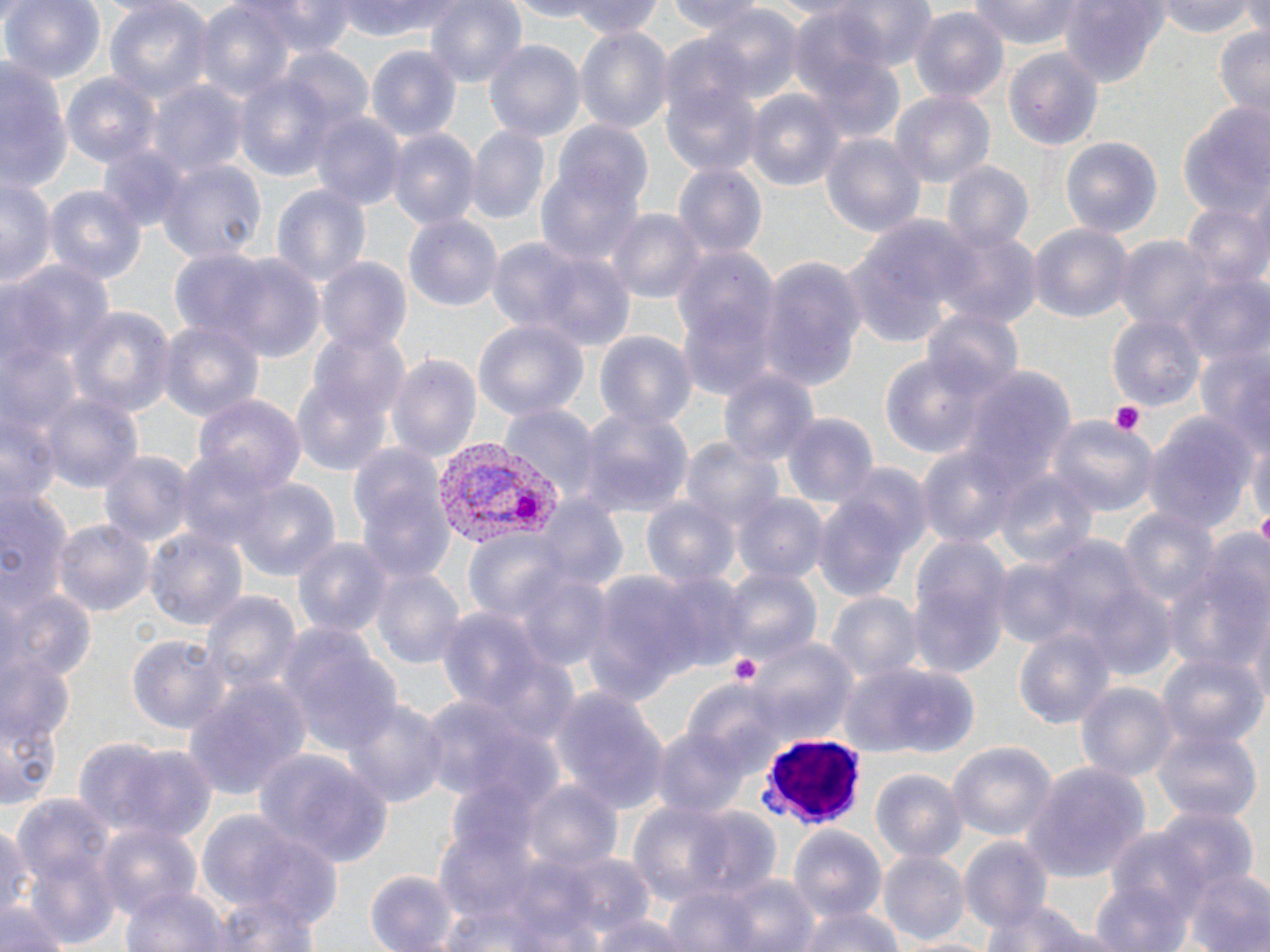
Summary:
  - Coordinate format: approximate bounding boxes as (x1, y1, x2, y2) in pixels
  - White blood cell locations: (763, 737, 868, 828)
  - Platelet locations: (1108, 399, 1145, 436), (1255, 510, 1270, 545), (727, 652, 765, 690)
  - Plasmodium vivax-infected red blood cell locations: (428, 436, 568, 551)
  - Uninfected red blood cell locations: (2, 0, 106, 85), (102, 0, 212, 106), (193, 0, 296, 104), (241, 0, 359, 56), (336, 0, 472, 42), (424, 0, 530, 90), (500, 0, 605, 20), (567, 0, 667, 39), (667, 0, 769, 37), (816, 0, 940, 72), (966, 0, 1088, 47), (1157, 0, 1261, 38), (1058, 1, 1173, 89), (701, 6, 802, 103), (910, 9, 1008, 106), (790, 13, 902, 136), (1213, 24, 1270, 121), (575, 29, 671, 131), (483, 39, 584, 146), (271, 43, 371, 142), (368, 45, 461, 142), (657, 45, 765, 175), (1004, 47, 1104, 152), (0, 56, 68, 196), (232, 60, 345, 180), (61, 74, 159, 168), (150, 82, 247, 179), (744, 88, 845, 194), (892, 91, 993, 188), (1176, 99, 1269, 219), (311, 112, 404, 210), (549, 118, 654, 227), (466, 127, 548, 224), (388, 128, 480, 232), (818, 130, 925, 237), (1059, 137, 1163, 241), (95, 142, 195, 233), (157, 158, 266, 265), (537, 160, 646, 269), (940, 160, 1033, 253), (673, 163, 766, 261), (0, 176, 54, 293), (270, 180, 372, 290), (42, 183, 148, 290), (1182, 199, 1270, 296), (609, 207, 702, 301), (403, 214, 503, 316), (850, 214, 975, 341), (1027, 222, 1134, 325), (935, 225, 1040, 328), (1114, 236, 1215, 332), (487, 238, 631, 349), (669, 241, 781, 398), (196, 253, 328, 362), (757, 257, 867, 391), (316, 258, 413, 357), (6, 263, 115, 369), (1184, 275, 1270, 372), (67, 306, 176, 422), (923, 308, 1026, 405), (1107, 313, 1204, 414), (156, 319, 263, 421), (472, 320, 585, 423), (305, 325, 410, 429), (592, 330, 695, 428), (3, 336, 83, 449), (1191, 341, 1270, 464), (880, 351, 988, 462), (387, 353, 482, 468), (958, 364, 1072, 499), (292, 365, 395, 479), (719, 366, 820, 474), (38, 390, 144, 498), (189, 393, 309, 502), (501, 404, 600, 503), (578, 405, 695, 517), (778, 411, 880, 511), (1140, 413, 1260, 537), (1047, 415, 1158, 521), (1247, 432, 1269, 540), (683, 438, 786, 540), (917, 446, 1018, 547), (175, 447, 282, 556), (97, 449, 196, 548), (994, 467, 1098, 571), (230, 476, 342, 584), (355, 479, 457, 587), (0, 484, 72, 617), (811, 491, 920, 605), (736, 493, 828, 585), (642, 497, 740, 592), (538, 498, 626, 592), (1115, 503, 1220, 617), (54, 519, 152, 619), (146, 529, 247, 635), (462, 530, 575, 628), (292, 533, 392, 640), (907, 535, 1011, 674), (1164, 550, 1270, 678), (370, 564, 467, 673), (514, 566, 614, 672), (717, 566, 821, 670), (652, 569, 748, 672), (583, 571, 702, 706), (1083, 584, 1178, 681), (0, 587, 95, 693), (200, 590, 301, 699), (827, 592, 920, 683), (1243, 598, 1270, 712), (437, 607, 546, 719), (277, 624, 406, 764), (1012, 626, 1114, 728), (740, 635, 859, 744), (129, 637, 230, 734), (1157, 649, 1267, 749), (2, 650, 76, 765), (840, 663, 979, 758), (185, 675, 312, 805), (1076, 680, 1175, 781), (0, 684, 64, 815), (551, 686, 670, 812), (420, 694, 551, 813), (343, 697, 448, 807), (650, 724, 756, 823), (1152, 724, 1264, 824), (75, 735, 217, 842), (945, 741, 1057, 841), (253, 750, 395, 867), (1023, 759, 1153, 886), (869, 767, 968, 863), (523, 777, 623, 870), (11, 795, 121, 944), (627, 801, 737, 907), (687, 806, 782, 899), (1151, 807, 1256, 902), (197, 809, 340, 927), (94, 820, 203, 919), (0, 822, 35, 927), (1097, 823, 1211, 930), (785, 825, 887, 922), (960, 837, 1054, 936), (520, 848, 659, 944), (880, 848, 969, 945), (790, 863, 893, 948), (1184, 866, 1270, 952), (364, 867, 460, 951), (673, 869, 823, 952), (1088, 881, 1192, 952), (120, 882, 227, 952), (205, 896, 325, 952), (982, 896, 1097, 952), (1, 901, 69, 952), (794, 904, 906, 952), (587, 908, 701, 952)
  - Slide-level diagnosis: Plasmodium vivax
  - Preparation: thin blood smear
  - Image size: 1270×952 pixels
  - Stain: May-Grünwald-Giemsa
  - Magnification: 1000x
  - Field of view: one of a larger specimen
  - Modality: light microscopy